Outline each blood parasite and name the species.
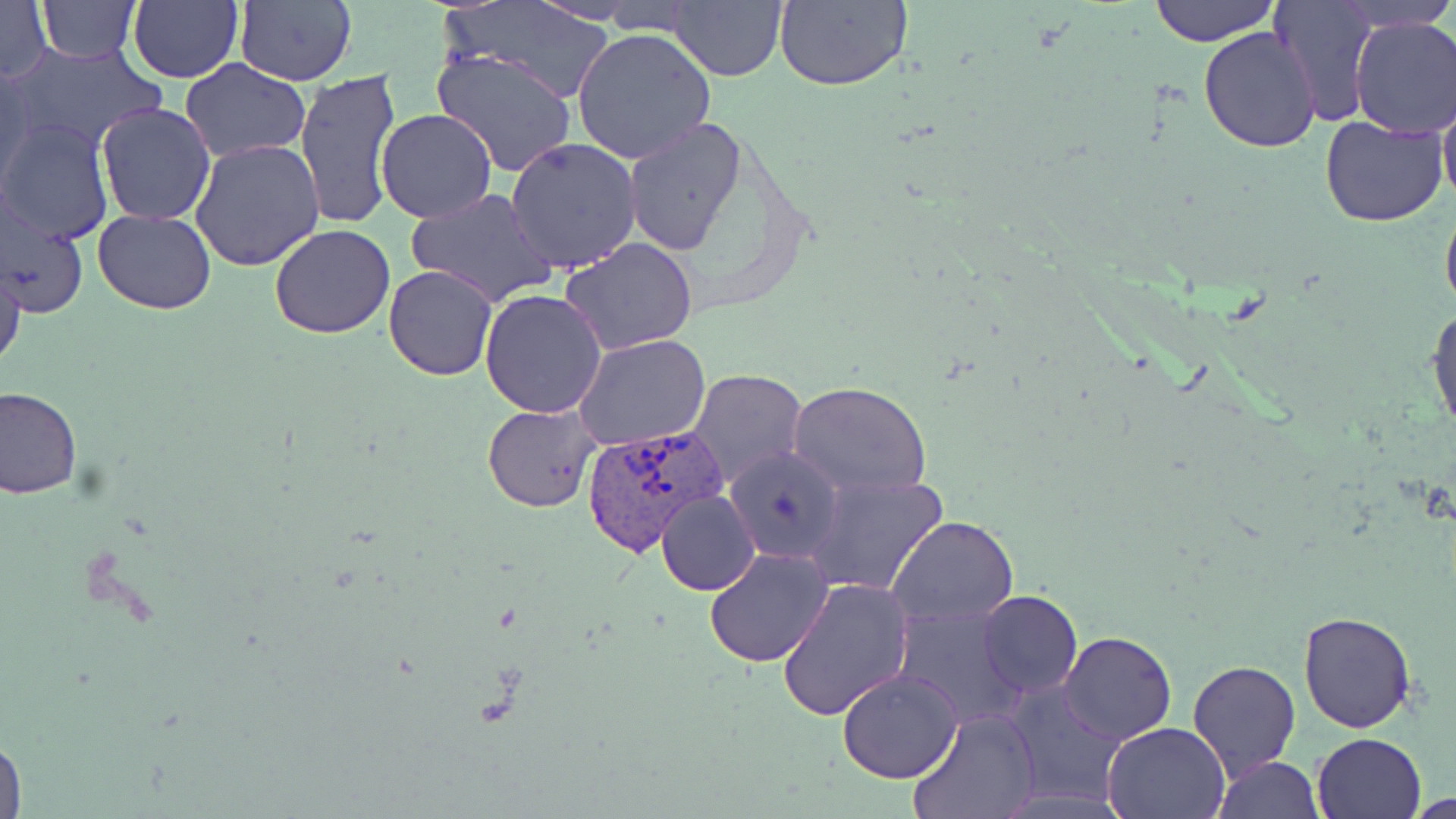

Approximate bounding boxes as (x1,y1)-(x2,y2) corner pairs in pixels.
Plasmodium vivax-infected red blood cells: (581,423)-(725,558).
No Plasmodium falciparum, Plasmodium ovale, Plasmodium malariae, Babesia divergens, or Trypanosoma brucei observed.

slide-level diagnosis = Plasmodium vivax
preparation = thin blood film
uninfected red blood cell locations = approximate bounding boxes as (x1,y1)-(x2,y2) corner pairs in pixels: (37,0)-(138,62), (129,0)-(243,84), (448,0)-(618,104), (667,0)-(788,83), (773,0)-(910,91), (1147,0)-(1279,46), (1338,0)-(1452,32), (234,1)-(356,85), (528,1)-(647,24), (1268,1)-(1379,126), (0,2)-(52,85), (1349,17)-(1456,138), (1199,26)-(1323,153), (571,27)-(715,164), (6,44)-(164,158), (430,47)-(578,178), (181,60)-(309,161), (0,66)-(38,190), (296,69)-(401,230), (1438,81)-(1456,219), (94,102)-(217,225), (375,110)-(497,224), (1319,114)-(1449,228), (1,118)-(116,243), (621,118)-(745,254), (505,136)-(641,273), (191,138)-(325,272), (406,187)-(556,311), (0,192)-(90,323), (1441,194)-(1456,323), (93,209)-(217,312), (269,224)-(395,339), (560,237)-(701,355), (0,254)-(24,376), (383,265)-(498,382), (479,288)-(608,417), (1427,303)-(1456,443), (576,334)-(711,453), (687,368)-(808,489), (790,383)-(931,497), (0,385)-(81,497), (483,402)-(601,512), (725,447)-(846,565), (806,471)-(948,597), (655,490)-(762,595), (887,515)-(1019,624), (704,547)-(834,667), (777,579)-(916,723), (978,590)-(1082,698), (893,603)-(1032,731), (1299,610)-(1416,734), (1059,631)-(1176,745), (1188,660)-(1301,780), (837,668)-(962,784), (1007,681)-(1131,805), (906,708)-(1041,819), (1102,721)-(1231,818), (1312,731)-(1426,817), (0,732)-(27,819), (1214,756)-(1325,818)
field of view = one of a larger specimen
modality = light microscopy
stain = May-Grünwald-Giemsa
image size = 1456×819 pixels
magnification = 1000x